Locate every Plasmodium parasite and every leukocyte.
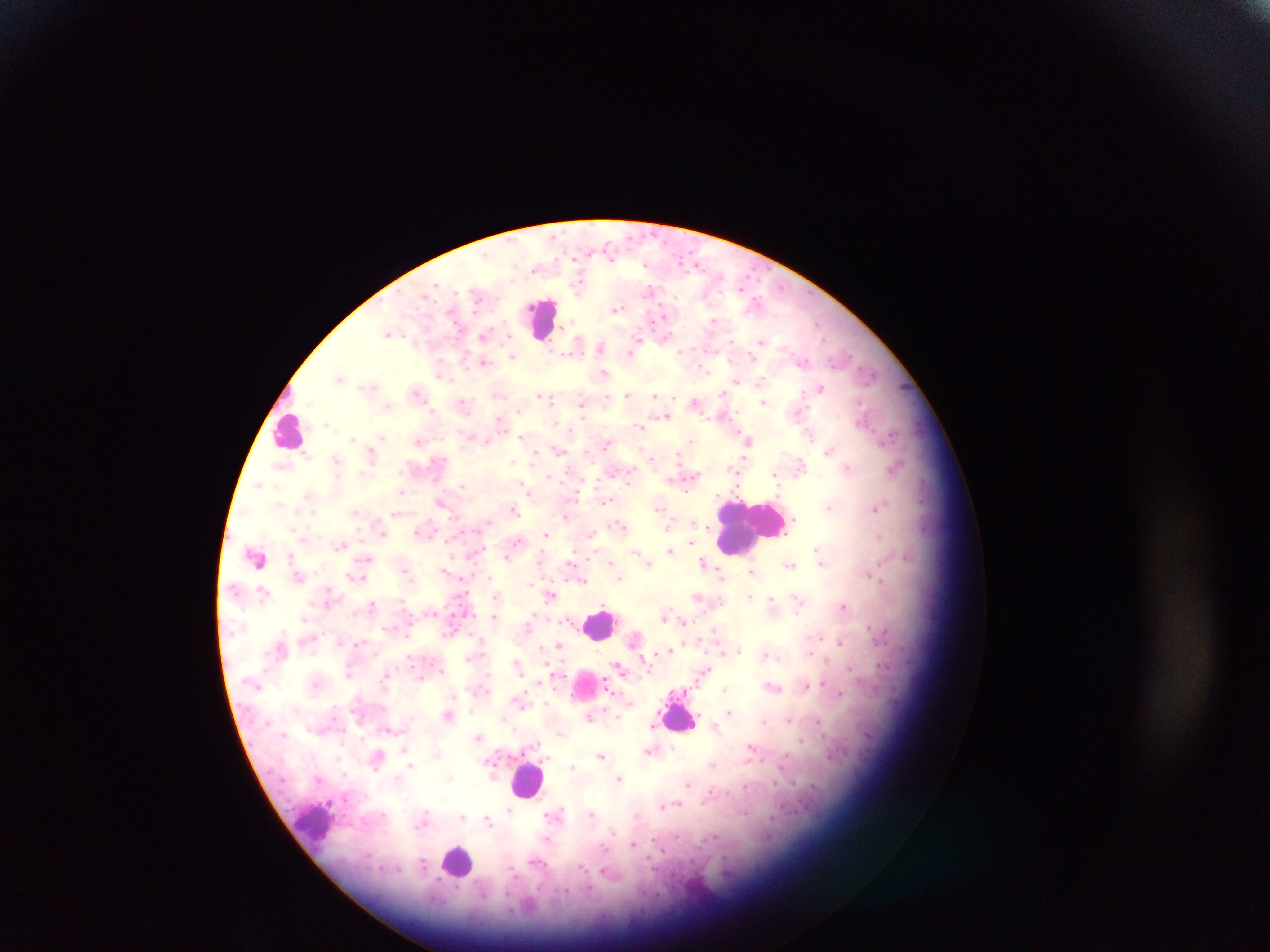
Approximate centers as (x, y) in pixels.
Plasmodium parasites: (610, 254), (697, 264), (743, 284), (578, 286), (435, 287), (649, 290), (477, 297), (617, 309), (662, 316), (713, 321), (388, 334), (483, 335), (665, 336), (509, 337), (636, 341), (731, 341), (762, 341), (577, 345), (601, 346), (681, 350), (511, 351), (631, 351), (513, 356), (751, 359), (802, 360), (483, 362), (603, 373), (871, 374), (340, 377), (736, 381), (760, 381), (370, 386), (820, 387), (416, 392), (722, 392), (627, 394), (540, 395), (655, 396), (545, 397), (551, 401), (694, 401), (462, 402), (763, 402), (858, 402), (582, 403), (386, 407), (519, 411), (797, 412), (665, 416), (500, 421), (326, 424), (641, 427), (809, 434), (353, 438), (381, 438), (522, 438), (691, 440), (749, 440), (418, 441), (487, 442), (606, 443), (558, 451), (829, 451), (534, 456), (651, 458), (513, 463), (800, 466), (848, 467), (732, 468), (896, 468), (774, 474), (550, 476), (691, 476), (629, 478), (259, 485), (463, 485), (523, 485), (528, 490), (401, 492), (577, 493), (606, 501), (828, 507), (659, 508), (876, 508), (514, 509), (395, 514), (566, 517), (794, 520), (693, 521), (488, 522), (620, 525), (668, 526), (707, 527), (382, 534), (546, 534), (591, 534), (880, 536), (691, 541), (517, 542), (341, 544), (816, 549), (636, 551), (669, 551), (368, 558), (507, 558), (611, 562), (703, 562), (571, 563), (790, 564), (648, 565), (820, 565), (444, 569), (407, 570), (753, 571), (720, 573), (362, 578), (619, 579), (880, 580), (582, 581), (551, 595), (496, 597), (697, 597), (750, 597), (771, 598), (798, 601), (372, 605), (843, 607), (798, 610), (666, 615), (494, 617), (683, 621), (870, 628), (821, 637), (359, 642), (840, 642), (559, 645), (670, 649), (740, 649), (722, 652), (809, 653), (766, 655), (778, 657), (518, 665), (618, 665), (851, 669), (443, 670), (705, 672), (349, 673), (384, 678), (824, 683), (806, 686), (774, 687), (725, 688), (840, 694), (520, 702), (546, 704), (471, 711), (729, 711), (448, 716), (617, 716), (590, 718), (503, 719), (788, 720), (818, 721), (763, 722), (651, 726), (715, 726), (389, 730), (515, 730), (477, 737), (538, 741), (801, 741), (341, 744), (672, 747), (750, 748), (405, 749), (648, 750), (601, 756), (713, 765), (410, 766), (572, 766), (619, 778), (688, 783), (746, 786), (677, 804), (662, 806), (509, 809), (561, 810), (549, 814), (592, 814), (462, 816), (488, 821), (547, 838), (655, 840), (633, 844), (603, 848), (423, 863).
Leukocytes: (541, 317), (290, 429), (748, 526), (256, 559), (601, 624), (680, 714), (528, 779), (314, 827), (458, 861).

Thick blood film. Photographed through a microscope with a mobile-phone camera. Single field of view. Image is 1270×952 pixels. Sample from Ghana.